Assess the morphology of the red blood cells.
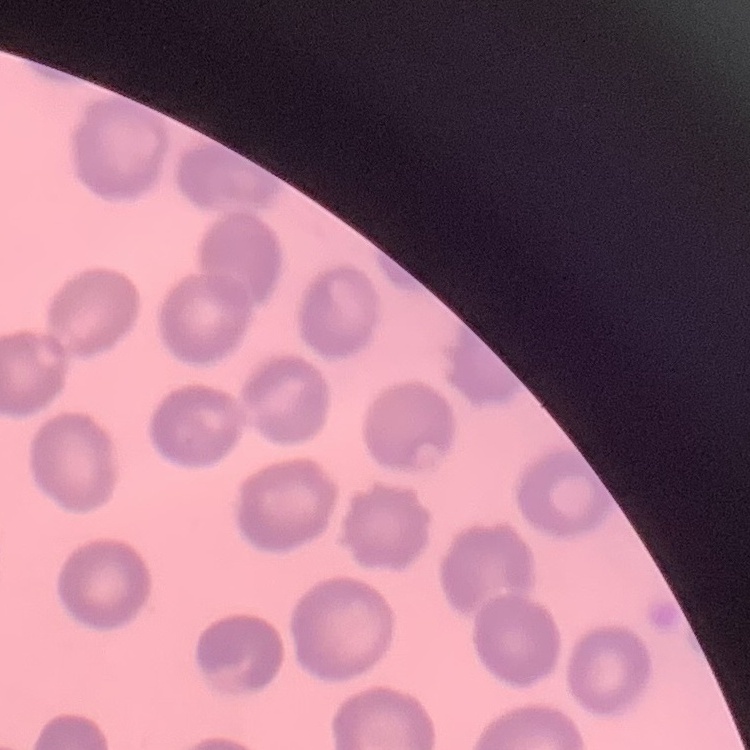
They show no rouleaux formation.

Thin peripheral smear. One tile cut from a larger photomicrograph. Stained with either Field's or Giemsa.